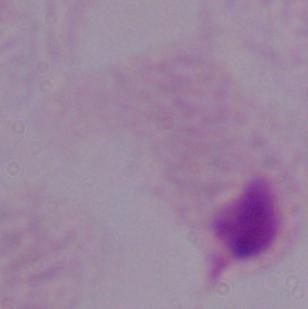
Micrograph. 1000x magnification. A trichomonad is seen.